State the blood parasite species.
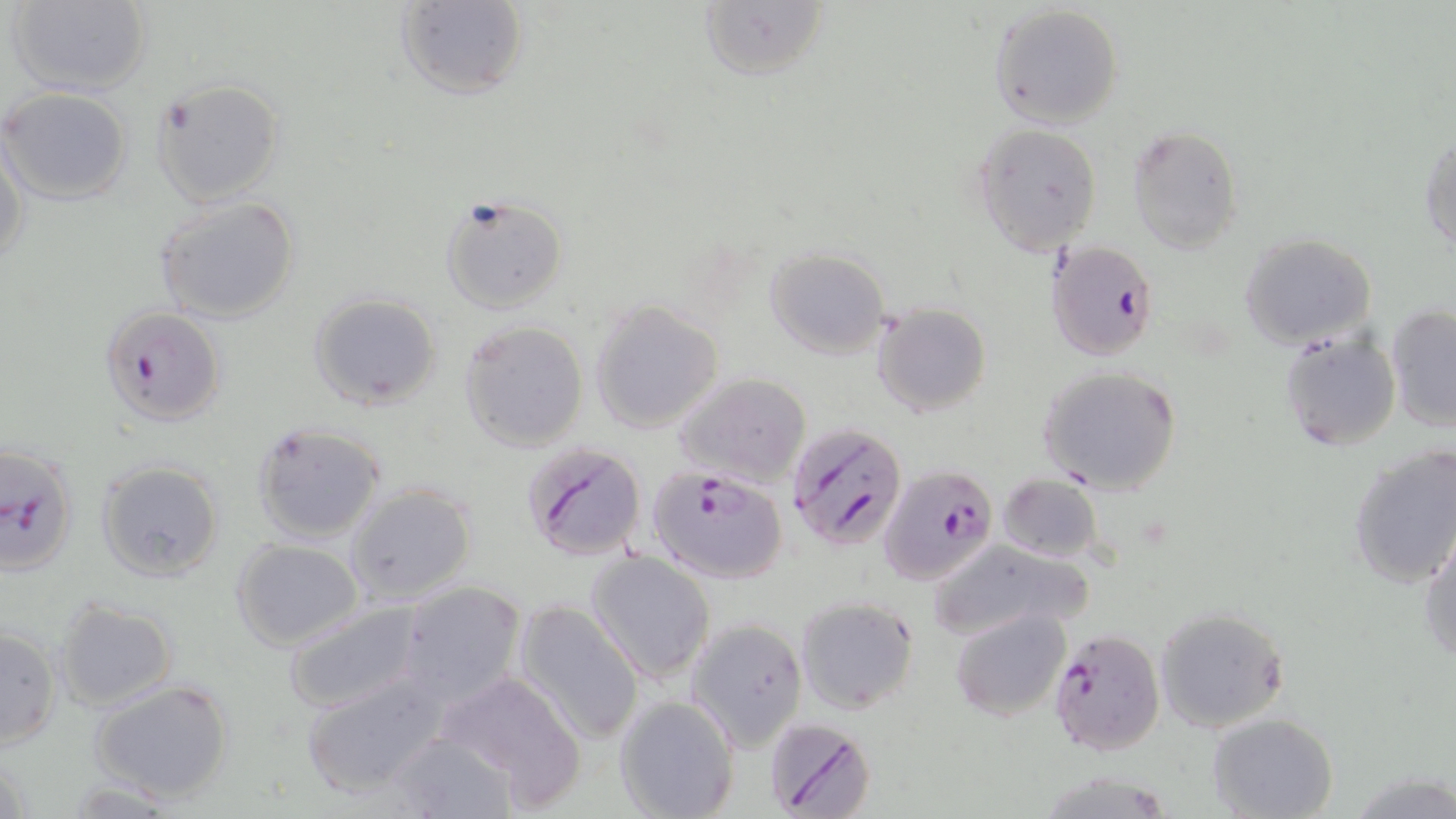

Plasmodium falciparum.

Approximate bounding boxes as named x1/y1/x2/y2 corners in pixels. Plasmodium falciparum-infected red blood cell locations: (x1=1047, y1=240, x2=1159, y2=360), (x1=99, y1=306, x2=224, y2=427), (x1=786, y1=423, x2=909, y2=551), (x1=0, y1=441, x2=80, y2=577), (x1=520, y1=442, x2=647, y2=563), (x1=879, y1=462, x2=997, y2=587), (x1=648, y1=465, x2=787, y2=584), (x1=1047, y1=629, x2=1164, y2=756), (x1=763, y1=714, x2=876, y2=819). Uninfected red blood cell locations: (x1=6, y1=0, x2=152, y2=96), (x1=395, y1=0, x2=526, y2=99), (x1=697, y1=1, x2=829, y2=83), (x1=989, y1=4, x2=1124, y2=129), (x1=149, y1=77, x2=284, y2=207), (x1=1, y1=87, x2=134, y2=205), (x1=972, y1=122, x2=1102, y2=254), (x1=1126, y1=126, x2=1245, y2=253), (x1=1419, y1=132, x2=1456, y2=255), (x1=1, y1=137, x2=26, y2=271), (x1=436, y1=194, x2=568, y2=315), (x1=155, y1=195, x2=303, y2=323), (x1=1239, y1=234, x2=1377, y2=350), (x1=764, y1=247, x2=890, y2=360), (x1=309, y1=293, x2=443, y2=409), (x1=589, y1=300, x2=725, y2=433), (x1=872, y1=303, x2=992, y2=418), (x1=1385, y1=304, x2=1456, y2=431), (x1=458, y1=319, x2=588, y2=452), (x1=1278, y1=329, x2=1402, y2=451), (x1=1037, y1=365, x2=1183, y2=495), (x1=676, y1=373, x2=808, y2=484), (x1=250, y1=422, x2=389, y2=544), (x1=1348, y1=444, x2=1456, y2=588), (x1=95, y1=459, x2=225, y2=581), (x1=998, y1=474, x2=1103, y2=563), (x1=343, y1=482, x2=478, y2=605), (x1=1419, y1=527, x2=1456, y2=664), (x1=230, y1=537, x2=364, y2=650), (x1=926, y1=538, x2=1095, y2=642), (x1=586, y1=550, x2=715, y2=683), (x1=397, y1=581, x2=525, y2=709), (x1=54, y1=597, x2=178, y2=711), (x1=279, y1=597, x2=426, y2=715), (x1=796, y1=597, x2=920, y2=716), (x1=512, y1=600, x2=645, y2=744), (x1=1154, y1=606, x2=1289, y2=733), (x1=951, y1=608, x2=1071, y2=722), (x1=688, y1=618, x2=807, y2=751), (x1=461, y1=625, x2=629, y2=780), (x1=1, y1=626, x2=62, y2=748), (x1=302, y1=670, x2=453, y2=800), (x1=432, y1=670, x2=583, y2=805), (x1=89, y1=677, x2=235, y2=803), (x1=614, y1=696, x2=740, y2=819), (x1=1207, y1=712, x2=1339, y2=819), (x1=387, y1=729, x2=515, y2=818), (x1=1039, y1=772, x2=1176, y2=818), (x1=57, y1=779, x2=187, y2=816). May-Grünwald-Giemsa-stained preparation. Optical microscopy. Captured at 1000x magnification. One field of a larger specimen. Thin blood smear. Image is 1456×819 pixels.